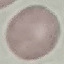

Summary:
  - Result: negative for malaria parasites
  - Capture: smartphone through the microscope eyepiece
  - Stain: Giemsa
  - Image type: automatically extracted cell patch, resized to 64 × 64 pixels
  - Preparation: thin blood smear